Locate every Plasmodium parasite.
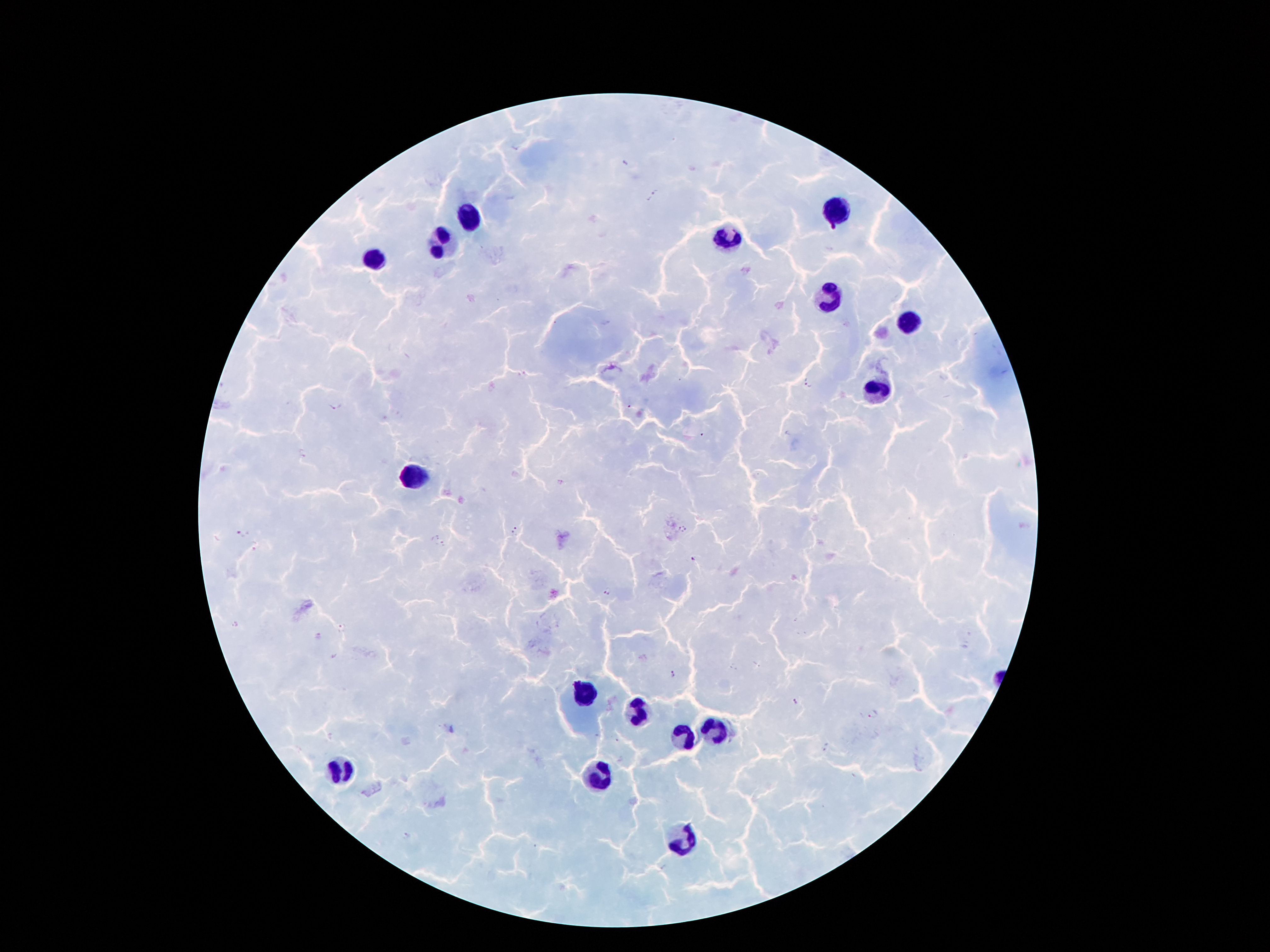

Approximate centers as (x, y) in pixels.
Plasmodium parasites: (515, 149), (654, 196), (808, 383), (333, 406), (630, 407), (701, 436), (302, 454), (515, 530), (683, 530), (240, 534), (254, 545), (441, 545), (691, 558), (607, 592), (236, 624), (340, 628), (318, 636), (672, 675), (795, 701), (873, 713), (826, 747), (406, 836).

image_size: 1270×952 pixels
field_of_view: one from this slide
magnification: 100x
patient_malaria_status: positive for Plasmodium falciparum
preparation: thick blood film
capture: smartphone camera through the microscope eyepiece
stain: Giemsa
leukocyte_locations: 'approximate centers as (x, y) in pixels: (835, 209), (471, 217), (731, 238), (441, 241), (372, 258), (828, 294), (909, 324), (876, 393), (416, 474), (584, 694), (640, 712), (714, 731), (683, 737), (342, 767), (598, 775), (686, 843)'